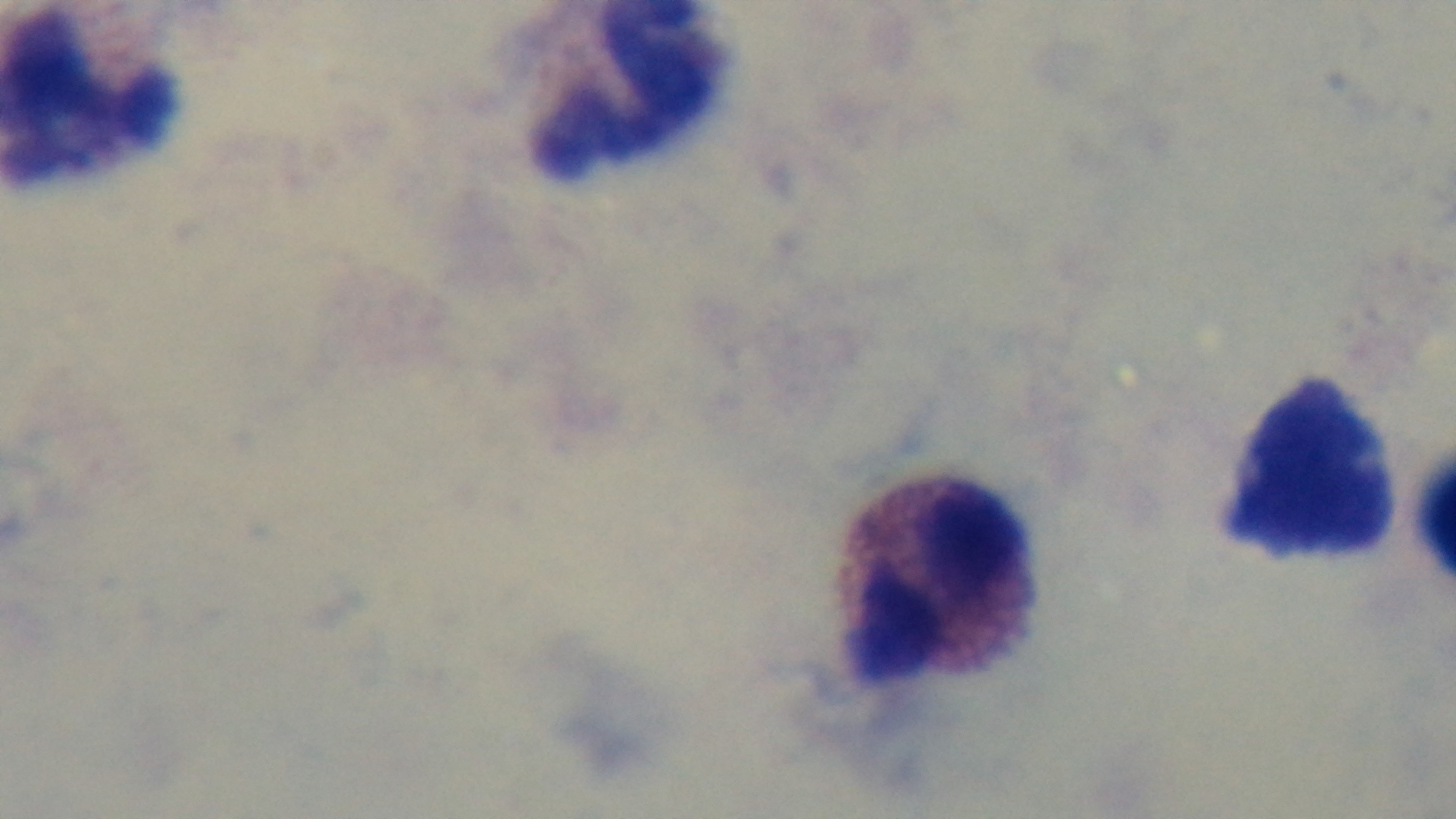
preparation: thick blood film
field_of_view: single
capture: mounted 4K digital camera
stain: Giemsa
modality: light microscopy
objective: 100x oil immersion
malaria_status: negative